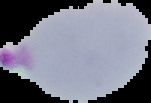
image size = 151×103 pixels
preparation = thin blood film
image type = segmented cell region with the area outside set to black
result = malaria parasites detected